Outline each blood parasite and name the species.
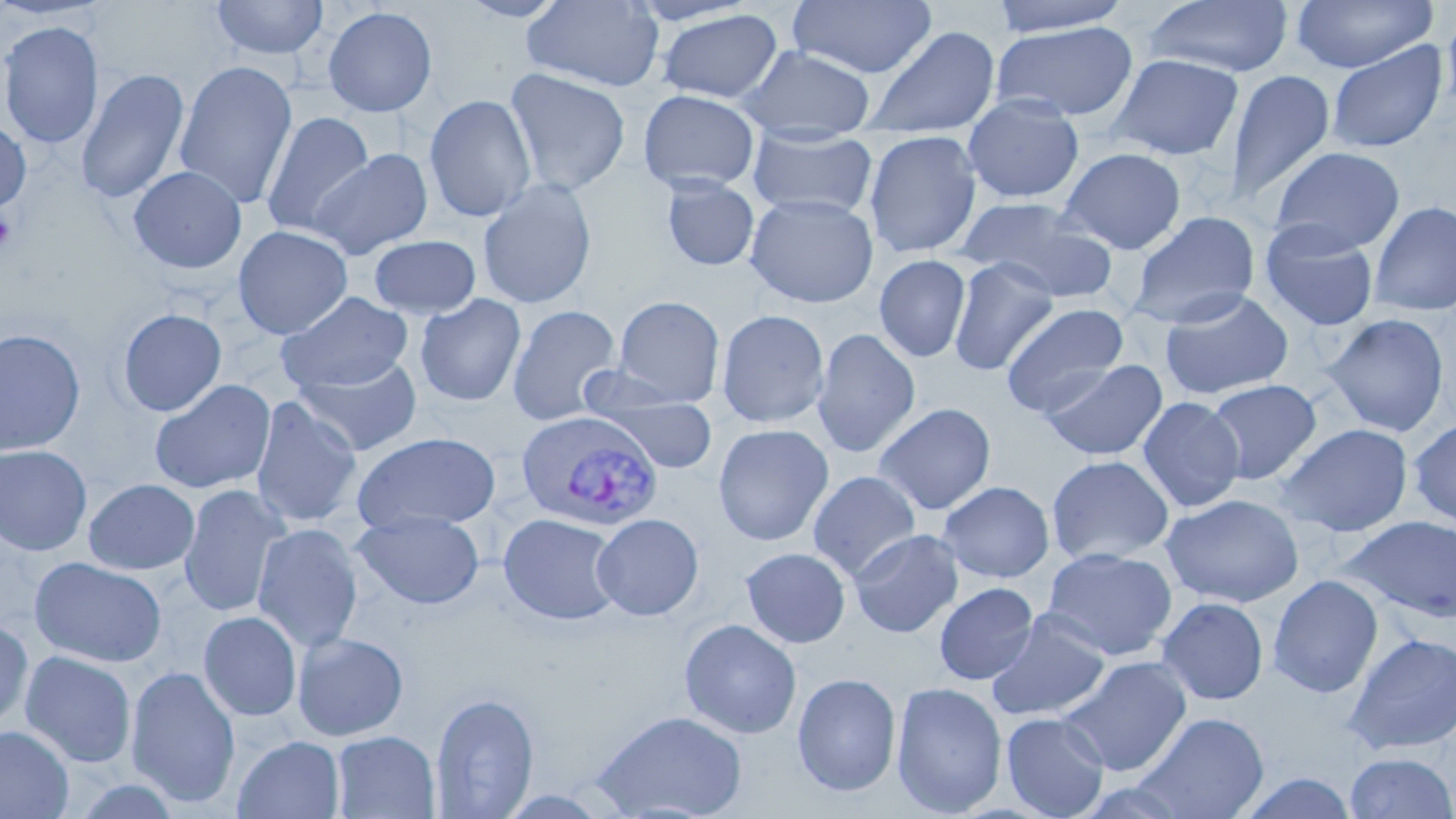
Approximate bounding boxes as (x1,y1)-(x2,y2) corner pairs in pixels.
Plasmodium vivax-infected red blood cells: (515,411)-(663,532).
No Plasmodium falciparum, Plasmodium ovale, Plasmodium malariae, Babesia divergens, or Trypanosoma brucei observed.

Uninfected red blood cell locations: (210,0)-(330,61), (455,0)-(572,23), (521,0)-(665,92), (787,0)-(937,79), (988,0)-(1133,37), (1143,0)-(1294,79), (1290,0)-(1437,74), (625,1)-(763,27), (1441,2)-(1456,120), (322,5)-(439,117), (655,9)-(784,104), (0,20)-(104,150), (991,22)-(1139,122), (859,25)-(1001,140), (1326,41)-(1448,154), (737,45)-(876,137), (1106,53)-(1245,161), (173,60)-(298,209), (76,67)-(191,205), (503,68)-(632,197), (1224,69)-(1335,206), (637,89)-(761,194), (423,94)-(537,223), (962,94)-(1085,204), (260,111)-(375,240), (0,119)-(31,213), (746,128)-(878,220), (863,130)-(982,259), (1269,146)-(1405,255), (1058,147)-(1187,255), (309,148)-(434,259), (128,165)-(247,274), (660,177)-(760,271), (477,178)-(598,310), (745,193)-(879,308), (958,197)-(1118,302), (1369,200)-(1456,317), (1126,210)-(1261,329), (1259,220)-(1380,332), (233,225)-(353,339), (368,235)-(481,319), (873,255)-(971,363), (948,257)-(1059,376), (1158,288)-(1294,401), (277,292)-(414,393), (415,294)-(526,407), (612,295)-(725,406), (1001,301)-(1129,417), (506,304)-(623,426), (118,308)-(227,416), (716,309)-(830,428), (1321,313)-(1450,437), (0,328)-(86,456), (811,328)-(921,458), (292,355)-(423,456), (1040,358)-(1168,461), (1204,378)-(1322,484), (149,379)-(276,494), (589,392)-(720,473), (249,396)-(363,529), (1137,396)-(1245,513), (873,403)-(996,515), (1408,416)-(1456,530), (712,423)-(834,546), (1276,423)-(1414,537), (352,432)-(502,532), (0,444)-(93,556), (1046,454)-(1174,566), (807,470)-(922,582), (83,478)-(200,575), (938,481)-(1055,583), (178,485)-(290,618), (1161,493)-(1303,607), (351,510)-(485,610), (498,512)-(624,626), (591,513)-(704,620), (1345,516)-(1456,623), (252,523)-(363,653), (848,528)-(964,638), (741,546)-(851,648), (1042,547)-(1178,661), (30,557)-(167,668), (1268,574)-(1383,699), (934,582)-(1039,685), (1156,596)-(1269,706), (986,610)-(1111,722), (198,611)-(302,721), (679,619)-(802,739), (0,620)-(34,731), (292,632)-(409,741), (1344,632)-(1456,756), (19,650)-(137,768), (1059,656)-(1193,776), (126,665)-(240,808), (792,673)-(901,797), (891,681)-(1008,816), (430,693)-(539,818), (590,710)-(749,819), (1001,712)-(1110,819), (1134,712)-(1269,818), (0,725)-(74,819), (331,731)-(440,819), (232,735)-(345,819), (1344,751)-(1456,818), (1237,771)-(1358,818). Platelet locations: (0,211)-(18,251). Slide-level diagnosis: Plasmodium vivax. 1000x magnification. Image is 1456×819 pixels. May-Grünwald-Giemsa-stained preparation. Optical microscopy. Single field of view. Thin blood film.